Locate every blood parasite and identify its species.
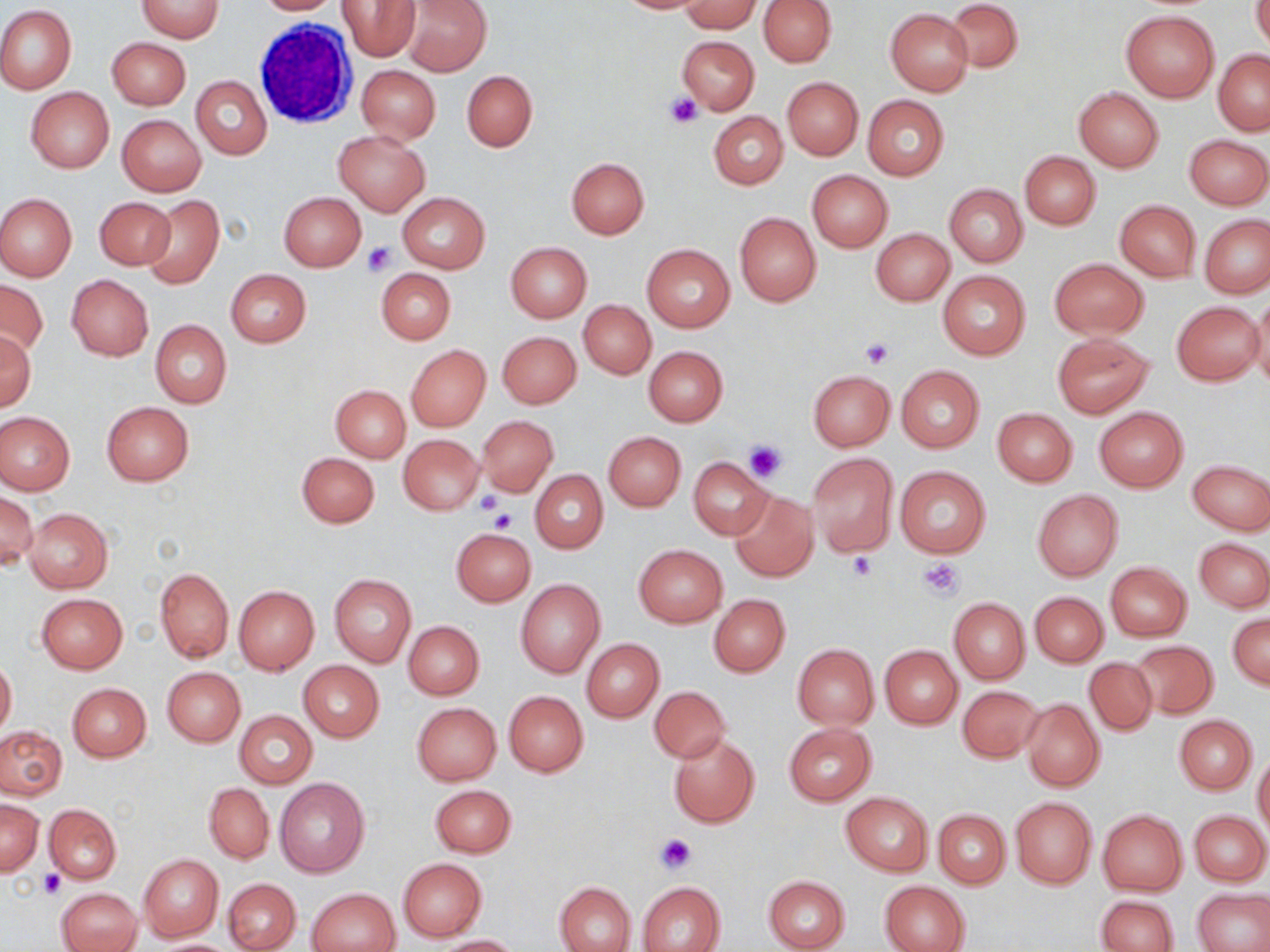

No blood parasites observed.

Approximate bounding boxes as (x1,y1)-(x2,y2) corner pairs in pixels. Uninfected red blood cell locations: (134,0)-(224,41), (252,0)-(340,15), (338,0)-(420,60), (402,0)-(491,75), (614,0)-(712,14), (758,0)-(837,67), (944,0)-(1022,73), (1252,0)-(1270,54), (681,2)-(762,32), (0,5)-(76,95), (885,9)-(973,96), (1120,10)-(1220,102), (677,35)-(759,115), (107,37)-(191,110), (1214,50)-(1270,134), (356,65)-(441,143), (462,70)-(536,151), (191,75)-(272,160), (781,77)-(862,159), (25,87)-(114,173), (1073,87)-(1164,172), (862,95)-(949,180), (709,111)-(788,189), (117,114)-(206,196), (334,130)-(430,214), (1185,134)-(1269,209), (1019,151)-(1100,229), (566,157)-(649,238), (807,170)-(892,252), (945,183)-(1027,268), (278,191)-(366,271), (0,193)-(77,281), (397,193)-(490,274), (94,196)-(175,271), (143,196)-(225,288), (1115,200)-(1201,282), (734,212)-(821,306), (1201,216)-(1270,297), (871,228)-(955,306), (505,242)-(591,322), (641,244)-(734,333), (1049,258)-(1148,339), (376,268)-(456,344), (225,269)-(311,347), (938,270)-(1029,358), (66,274)-(154,360), (0,280)-(48,357), (1250,292)-(1270,392), (578,300)-(655,379), (1171,301)-(1263,386), (150,319)-(232,408), (1,330)-(36,411), (498,332)-(581,408), (1051,333)-(1153,419), (405,343)-(490,432), (643,346)-(728,426), (896,365)-(984,452), (808,370)-(895,451), (329,384)-(410,462), (101,401)-(194,485), (1094,406)-(1188,491), (992,408)-(1077,485), (1,412)-(75,495), (477,416)-(559,497), (603,432)-(685,511), (399,435)-(484,514), (297,452)-(380,528), (807,452)-(899,556), (688,456)-(773,540), (1187,458)-(1269,536), (895,465)-(991,559), (530,470)-(607,554), (1032,489)-(1123,580), (730,490)-(818,582), (0,491)-(37,571), (24,508)-(113,593), (452,528)-(535,606), (1194,537)-(1270,612), (634,544)-(728,627), (1106,562)-(1191,641), (155,567)-(233,662), (329,574)-(418,668), (515,579)-(606,679), (233,585)-(320,675), (1030,592)-(1108,666), (37,593)-(128,673), (708,594)-(790,676), (948,597)-(1029,683), (1228,613)-(1269,690), (403,621)-(484,699), (582,638)-(664,722), (1130,641)-(1219,720), (792,644)-(878,728), (880,645)-(963,729), (1,656)-(16,739), (1083,657)-(1157,736), (298,661)-(383,742), (161,667)-(245,747), (67,683)-(151,762), (956,685)-(1043,763), (649,686)-(730,763), (503,691)-(588,776), (1021,698)-(1105,791), (411,702)-(502,786), (234,711)-(317,789), (1174,716)-(1257,794), (783,723)-(876,806), (0,725)-(67,800), (668,733)-(760,828), (1253,754)-(1270,840), (276,778)-(369,879), (204,784)-(274,863), (430,784)-(515,857), (841,792)-(933,876), (1010,797)-(1096,889), (0,799)-(43,876), (45,804)-(121,884), (933,809)-(1011,888), (1097,810)-(1187,895), (1191,811)-(1268,886), (138,853)-(224,942), (398,858)-(487,942), (763,874)-(850,952), (224,878)-(299,951), (881,880)-(969,951), (555,881)-(636,952), (637,881)-(725,952), (306,887)-(400,952), (56,888)-(141,952), (1194,889)-(1270,951), (1094,895)-(1180,951), (436,935)-(521,952), (149,939)-(239,951). White blood cell locations: (253,18)-(357,128). Platelet locations: (667,92)-(702,128), (362,241)-(396,276), (860,337)-(893,368), (743,439)-(787,481), (473,491)-(506,517), (489,508)-(518,533), (848,552)-(877,581), (919,557)-(965,600), (655,834)-(695,873), (39,869)-(66,898). Slide-level diagnosis: no evidence of blood parasites. 1000x magnification. May-Grünwald-Giemsa-stained preparation. Optical microscopy. Thin blood film. Image is 1270×952 pixels. One field of a larger specimen.